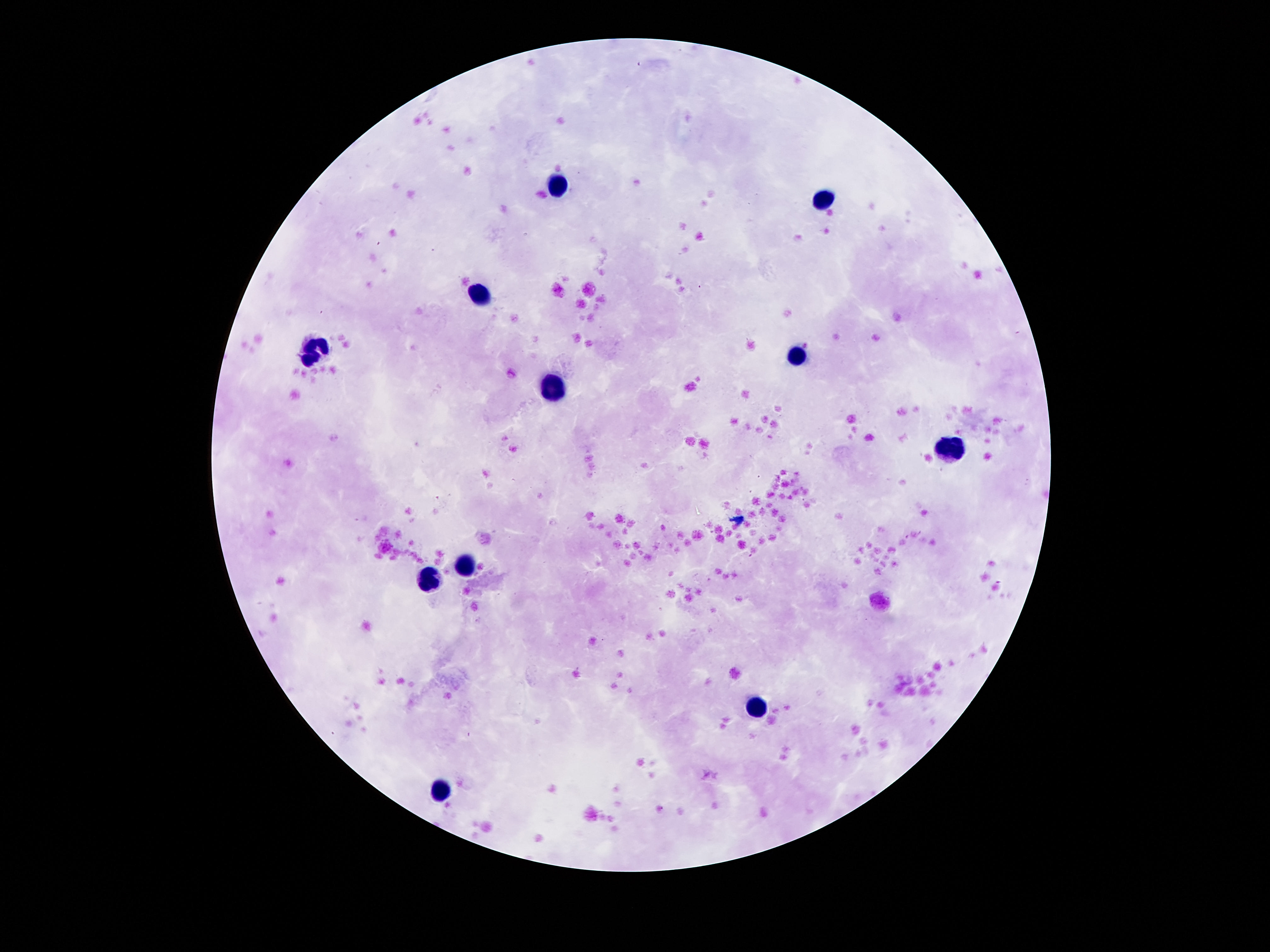

Approximate centers as {x, y} in pixels.
Summary:
  - Leukocyte locations: {559, 180}, {822, 196}, {481, 298}, {318, 353}, {798, 357}, {552, 391}, {952, 448}, {466, 562}, {426, 575}, {756, 707}, {439, 793}
  - Field of view: one from this slide
  - Image size: 1270×952 pixels
  - Patient malaria status: negative
  - Capture: smartphone camera through the microscope eyepiece
  - Preparation: thick blood smear
  - Stain: Giemsa
  - Magnification: 100x